Describe the morphology of the erythrocytes.
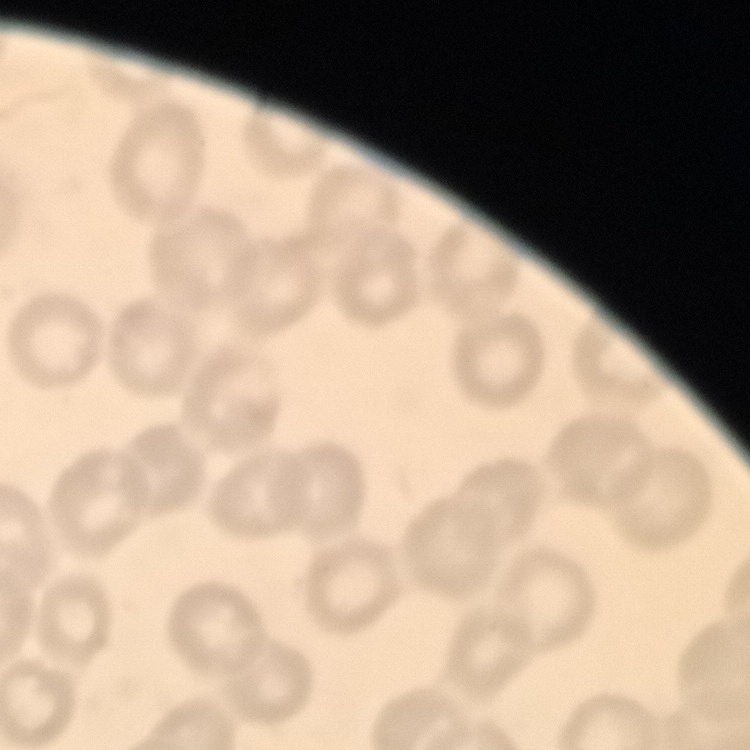
They show no rouleaux formation.

preparation: thin blood smear
image_type: square crop of a larger photomicrograph
stain: Field's or Giemsa